Locate every blood parasite and identify its species.
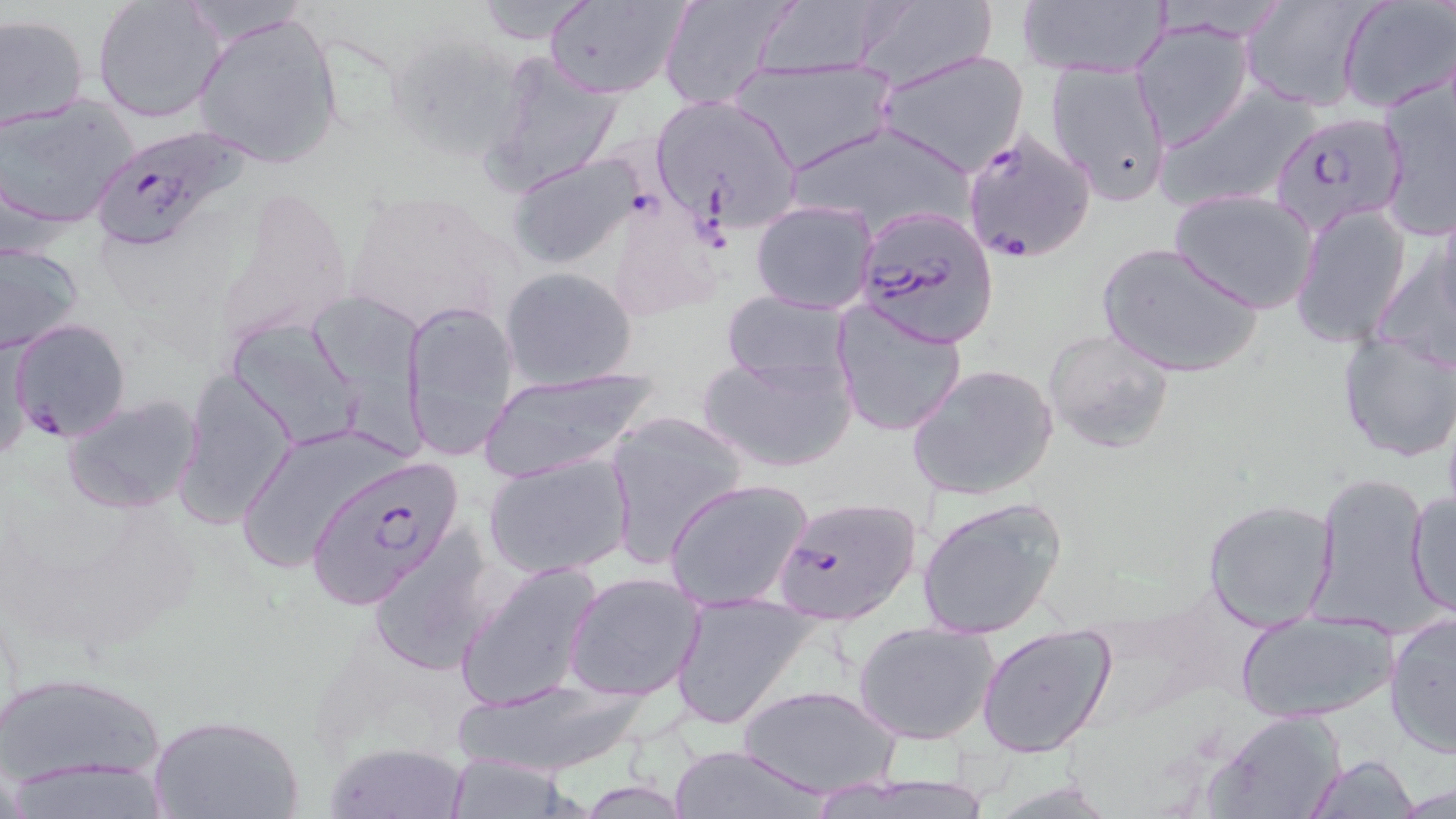
Approximate bounding boxes as [x1, y1, x2, y2] in pixels.
Plasmodium falciparum-infected red blood cells: [1269, 113, 1407, 237], [89, 126, 249, 253], [962, 130, 1095, 263], [849, 212, 995, 354], [10, 319, 131, 444], [303, 455, 467, 611], [769, 496, 922, 626].
No Plasmodium ovale, Plasmodium malariae, Plasmodium vivax, Babesia divergens, or Trypanosoma brucei observed.

Summary:
  - Uninfected red blood cell locations: [658, 0, 798, 110], [746, 0, 898, 78], [1016, 0, 1169, 78], [1240, 0, 1376, 111], [1338, 0, 1454, 114], [93, 1, 226, 124], [469, 1, 596, 44], [543, 1, 688, 99], [850, 3, 999, 88], [191, 10, 344, 170], [0, 13, 89, 132], [1133, 20, 1254, 151], [387, 30, 528, 160], [875, 49, 1030, 177], [478, 53, 626, 198], [726, 57, 897, 175], [1044, 58, 1175, 209], [1378, 77, 1456, 237], [1160, 83, 1318, 212], [647, 93, 804, 233], [2, 95, 139, 229], [781, 120, 978, 240], [506, 151, 645, 271], [340, 188, 523, 339], [1171, 189, 1319, 314], [607, 190, 727, 322], [750, 200, 877, 314], [1290, 202, 1411, 349], [1432, 205, 1456, 331], [1099, 239, 1266, 379], [1373, 240, 1456, 368], [0, 242, 85, 354], [500, 266, 638, 389], [719, 291, 854, 389], [402, 298, 520, 463], [831, 299, 968, 438], [229, 320, 365, 450], [1043, 328, 1176, 454], [1336, 329, 1455, 462], [697, 347, 856, 473], [907, 362, 1059, 501], [178, 366, 296, 526], [473, 366, 662, 478], [62, 395, 205, 515], [604, 409, 752, 569], [233, 426, 397, 576], [482, 451, 636, 579], [1310, 469, 1435, 636], [662, 476, 815, 612], [1405, 487, 1455, 619], [916, 494, 1069, 639], [1202, 498, 1338, 631], [367, 528, 498, 677], [455, 560, 602, 712], [564, 570, 707, 702], [668, 589, 817, 731], [1235, 607, 1396, 724], [1384, 614, 1455, 760], [853, 621, 1000, 745], [974, 625, 1118, 759], [0, 669, 168, 790], [446, 676, 654, 779], [736, 683, 902, 798], [1210, 709, 1346, 819], [150, 712, 303, 819], [325, 740, 470, 818], [664, 743, 832, 818], [442, 754, 581, 818], [1305, 755, 1421, 818], [6, 761, 181, 819], [812, 769, 996, 819]
  - Slide-level diagnosis: Plasmodium falciparum
  - Stain: May-Grünwald-Giemsa
  - Field of view: single
  - Image size: 1456×819 pixels
  - Magnification: 1000x
  - Modality: optical microscopy
  - Preparation: thin blood smear